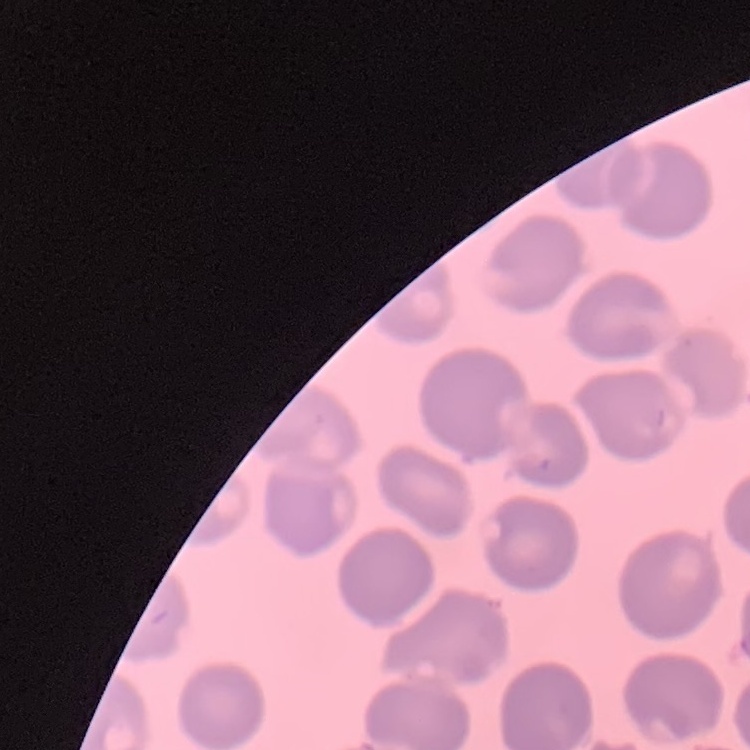

Summary:
  - Red blood cell morphology: no rouleaux formation
  - Image type: one tile cut from a larger photomicrograph
  - Preparation: thin blood smear
  - Stain: Field's or Giemsa